Classify this cell by malaria status.
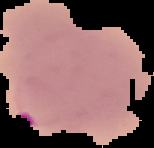

Parasitized.

{
  "image_type": "segmented cell region on a black background",
  "image_size": "154×148 pixels",
  "preparation": "thin blood film"
}